Identify the cell.
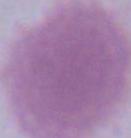
An erythrocyte.

magnification = 1000x
modality = micrograph